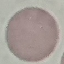

Result: no malaria parasites detected. Giemsa-stained preparation. Acquired by smartphone through the microscope eyepiece. Automatically extracted cell patch, resized to 64 × 64 pixels. Thin blood film.